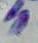

modality = micrograph
magnification = 1000x
identification = Toxoplasma gondii